Comment on the morphology of the red blood cells.
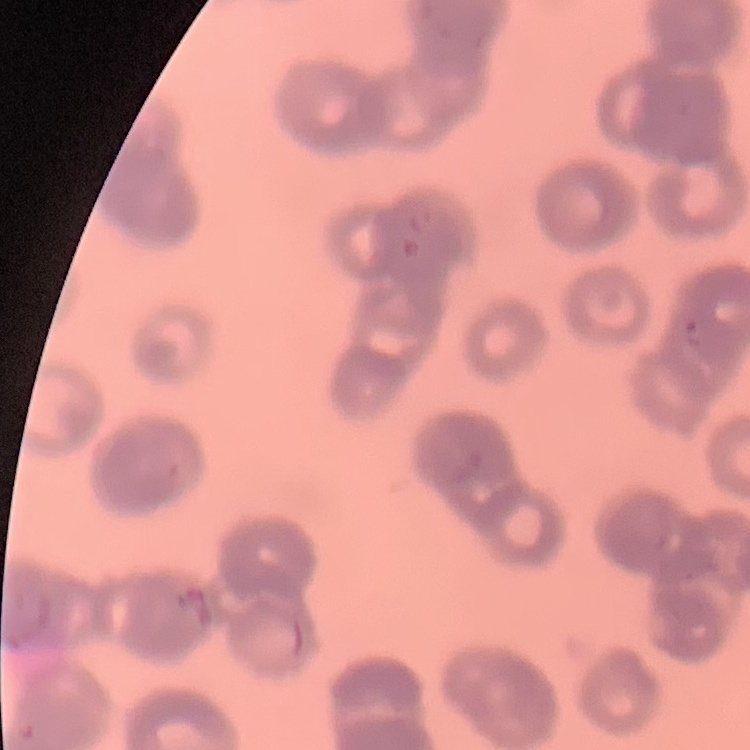
They show rouleaux formation.

Summary:
  - Stain: Field's or Giemsa
  - Image type: square crop of a larger photomicrograph
  - Preparation: thin blood film